Point out each Plasmodium parasite.
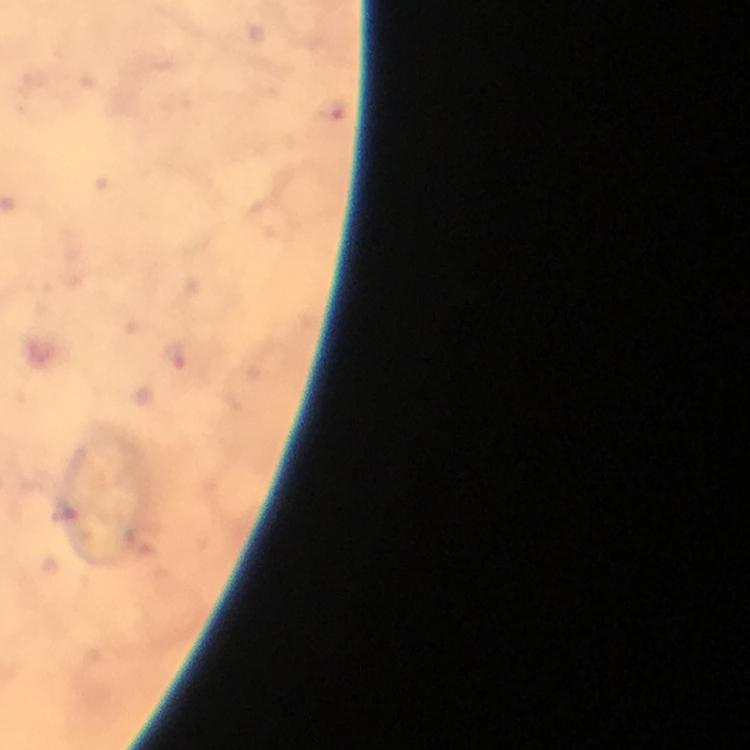

Approximate object centers, in pixels from the top-left corner.
Plasmodium parasites: (x=173, y=355).

immersion oil = used
image size = 750×750 pixels
preparation = thick blood smear
cropped from = one field of view
stain = Giemsa
context = from a diagnostic examination for malaria
magnification = 100x
capture = smartphone photograph through a microscope